Outline each blood parasite and name the species.
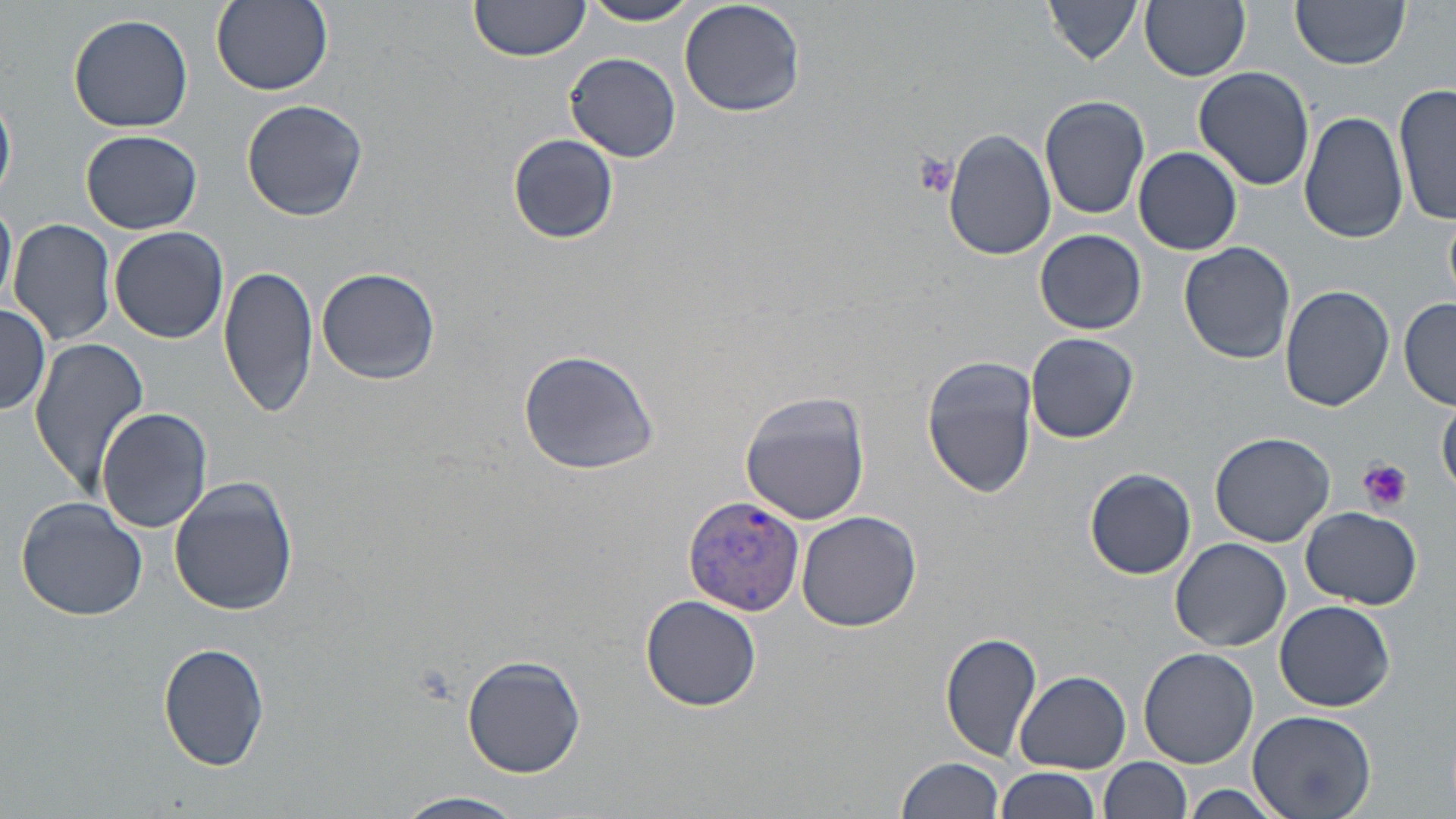
Approximate bounding boxes as (x1,y1)-(x2,y2) corner pairs in pixels.
Plasmodium vivax-infected red blood cells: (685,497)-(806,615).
No Plasmodium falciparum, Plasmodium ovale, Plasmodium malariae, Babesia divergens, or Trypanosoma brucei observed.

Summary:
  - Uninfected red blood cell locations: (211,0)-(333,95), (469,0)-(590,62), (678,0)-(806,119), (1139,0)-(1251,81), (582,1)-(704,25), (1046,1)-(1144,64), (1291,2)-(1408,70), (67,12)-(197,134), (566,52)-(682,163), (1192,65)-(1316,190), (1395,82)-(1456,225), (0,86)-(16,207), (1039,94)-(1150,219), (240,99)-(367,221), (1299,111)-(1410,245), (81,129)-(201,234), (944,130)-(1055,262), (508,134)-(618,244), (1132,146)-(1243,255), (0,193)-(16,314), (9,217)-(117,347), (109,225)-(229,344), (1035,229)-(1147,334), (1179,241)-(1298,365), (221,265)-(319,419), (314,266)-(441,387), (1280,284)-(1393,411), (1399,296)-(1456,410), (0,302)-(52,418), (1025,332)-(1138,444), (28,337)-(152,496), (517,347)-(661,475), (922,355)-(1037,498), (739,392)-(872,524), (1438,402)-(1456,497), (96,406)-(215,534), (1210,431)-(1335,548), (1084,467)-(1196,580), (168,475)-(298,617), (14,496)-(149,621), (1299,505)-(1423,608), (797,509)-(922,632), (1169,539)-(1292,652), (640,595)-(764,712), (1275,600)-(1394,712), (940,629)-(1044,761), (158,640)-(271,773), (1138,646)-(1258,769), (460,654)-(587,778), (1016,671)-(1130,773), (1246,709)-(1374,818), (1102,757)-(1192,819), (897,758)-(1006,819), (993,767)-(1101,819), (1180,785)-(1287,819), (396,792)-(531,817)
  - Platelet locations: (908,148)-(959,200), (1357,460)-(1412,513)
  - Slide-level diagnosis: Plasmodium vivax
  - Magnification: 1000x
  - Field of view: single
  - Modality: light microscopy
  - Stain: May-Grünwald-Giemsa
  - Preparation: thin blood smear
  - Image size: 1456×819 pixels